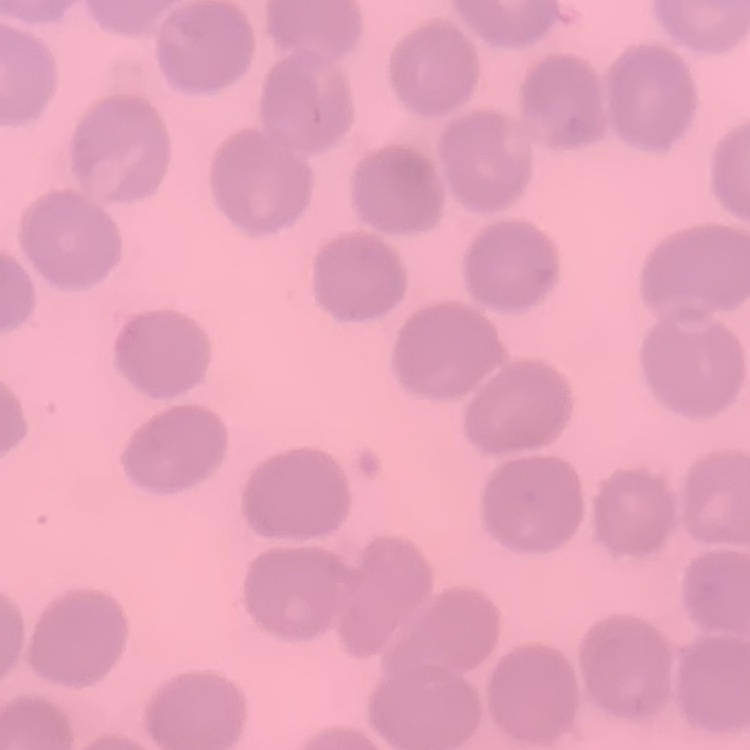
erythrocyte_morphology: no rouleaux formation
preparation: thin blood film
stain: Field's or Giemsa
image_type: square crop of a larger photomicrograph